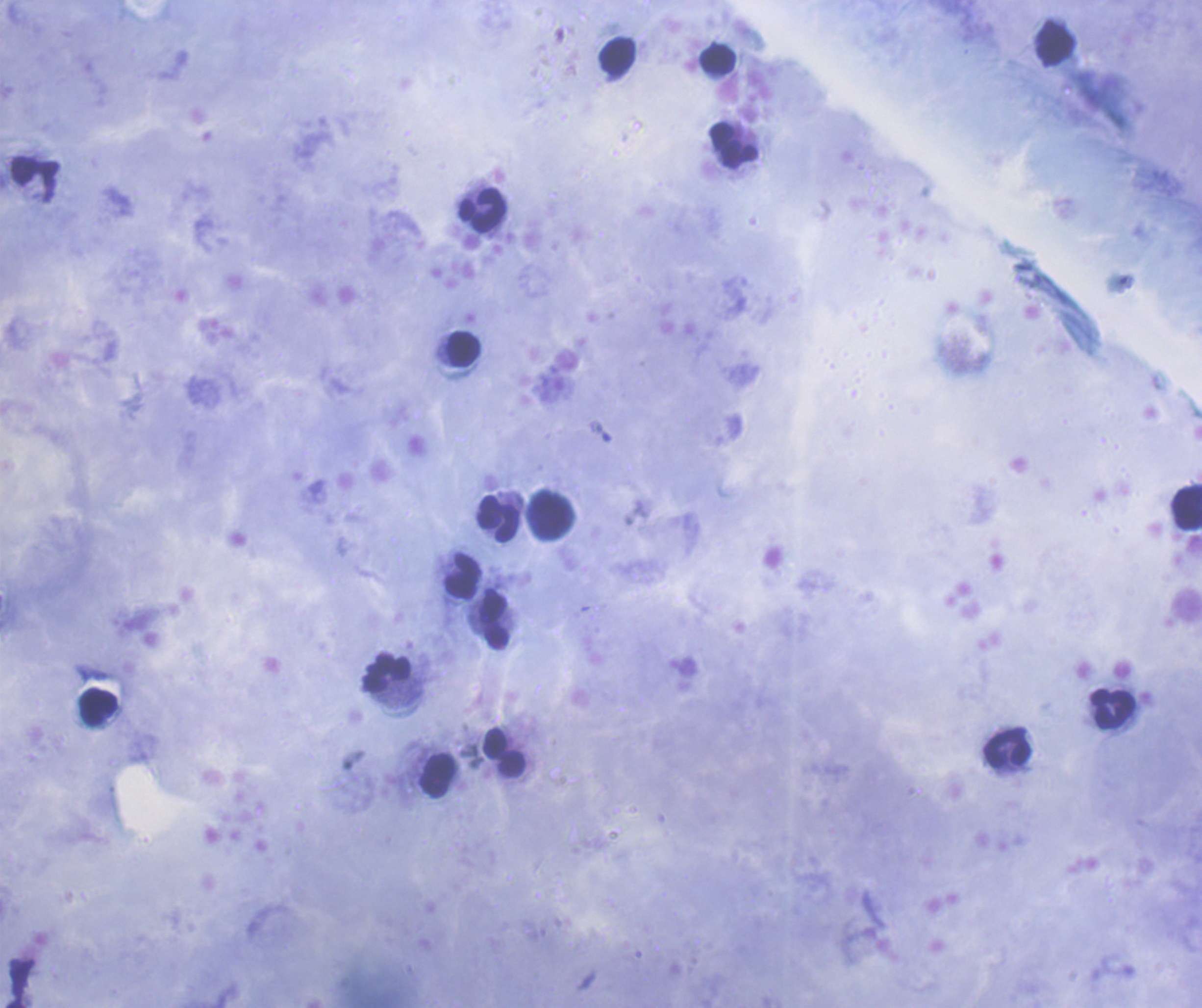
Approximate centers as {x, y} in pixels. Leukocyte locations: {1054, 44}, {618, 55}, {717, 60}, {733, 146}, {482, 210}, {464, 349}, {1187, 506}, {550, 515}, {499, 520}, {462, 576}, {494, 623}, {387, 673}, {98, 707}, {1112, 709}, {494, 743}, {1007, 749}, {512, 765}, {438, 775}. Thick blood smear. Previously used in an actual diagnosis. Background quality: satisfactory. One field from this slide. Romanowsky-stained preparation. 100x magnification. Result: no malaria parasites seen. Image is 1202×1008 pixels. Coloration quality: good.